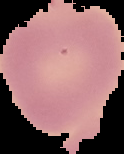

image type = segmented cell region on a black background
malaria status = uninfected
preparation = thin blood film
image size = 124×154 pixels